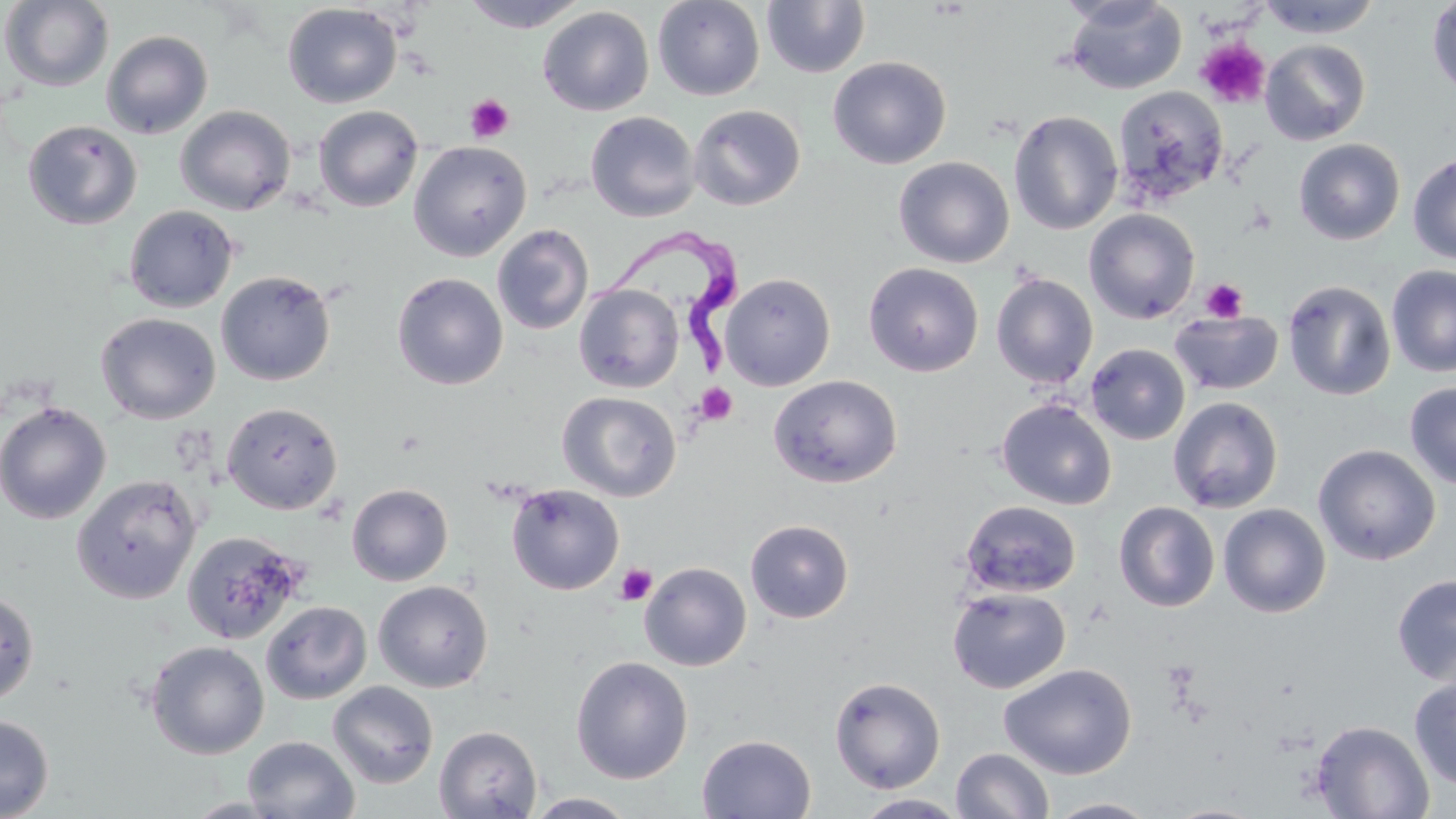
Approximate bounding boxes as (x1,y1)-(x2,y2) corner pairs in pixels. Uninfected red blood cell locations: (1,0)-(114,92), (459,0)-(590,32), (652,0)-(765,101), (1063,0)-(1187,94), (1256,0)-(1382,38), (1426,0)-(1456,99), (762,1)-(871,78), (282,3)-(402,109), (537,6)-(655,116), (101,30)-(213,139), (1260,40)-(1371,146), (828,56)-(951,169), (1112,86)-(1229,205), (688,104)-(806,211), (175,105)-(296,215), (313,105)-(424,212), (1008,110)-(1123,235), (585,111)-(700,222), (23,120)-(142,230), (1294,138)-(1405,245), (409,141)-(531,261), (1408,154)-(1456,265), (893,157)-(1015,268), (124,205)-(239,312), (1084,208)-(1200,324), (492,224)-(594,335), (863,262)-(984,377), (1386,265)-(1456,377), (216,270)-(337,386), (392,272)-(508,390), (720,272)-(836,391), (991,273)-(1098,389), (1283,280)-(1396,400), (574,284)-(684,393), (1170,311)-(1284,396), (96,313)-(221,424), (1086,343)-(1190,445), (768,374)-(903,488), (1404,382)-(1456,489), (558,391)-(682,502), (1168,396)-(1283,513), (996,399)-(1117,510), (0,401)-(112,524), (222,402)-(343,514), (1313,443)-(1441,565), (72,474)-(202,604), (346,483)-(453,585), (506,483)-(625,595), (961,500)-(1081,597), (1114,501)-(1220,612), (1218,503)-(1331,618), (745,519)-(854,623), (181,530)-(306,645), (639,562)-(752,671), (1392,574)-(1456,685), (373,580)-(493,692), (947,587)-(1071,693), (0,590)-(40,707), (262,601)-(371,704), (146,641)-(269,759), (570,656)-(693,784), (1000,663)-(1137,779), (829,676)-(946,794), (1408,676)-(1456,790), (327,681)-(439,789), (0,714)-(54,818), (1310,719)-(1434,818), (434,724)-(542,818), (697,734)-(816,818), (242,736)-(360,818), (951,748)-(1054,819), (525,792)-(637,818), (854,793)-(969,819), (182,797)-(291,818), (1044,797)-(1161,818). Trypanosoma brucei locations: (582,215)-(751,373). Platelet locations: (1195,38)-(1271,109), (465,93)-(515,143), (1201,278)-(1248,323), (695,383)-(738,425), (615,563)-(657,605). Slide-level diagnosis: Trypanosoma brucei. Light microscopy. Image is 1456×819 pixels. May-Grünwald-Giemsa-stained preparation. Single field of view. 1000x magnification. Thin blood film.